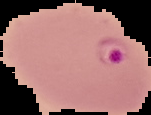 Cell region segmented out of the field of view; the surrounding area is masked to black. From a thin blood film. Malaria status: parasitized. Image is 151×115 pixels.